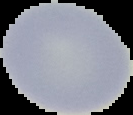 Malaria status: uninfected. Image is 133×115 pixels. From a thin blood film. Cell region segmented out of the field of view; the surrounding area is masked to black.